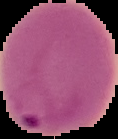

Summary:
  - Image type: segmented cell region with the area outside set to black
  - Image size: 118×139 pixels
  - Preparation: thin blood smear
  - Result: malaria parasites detected